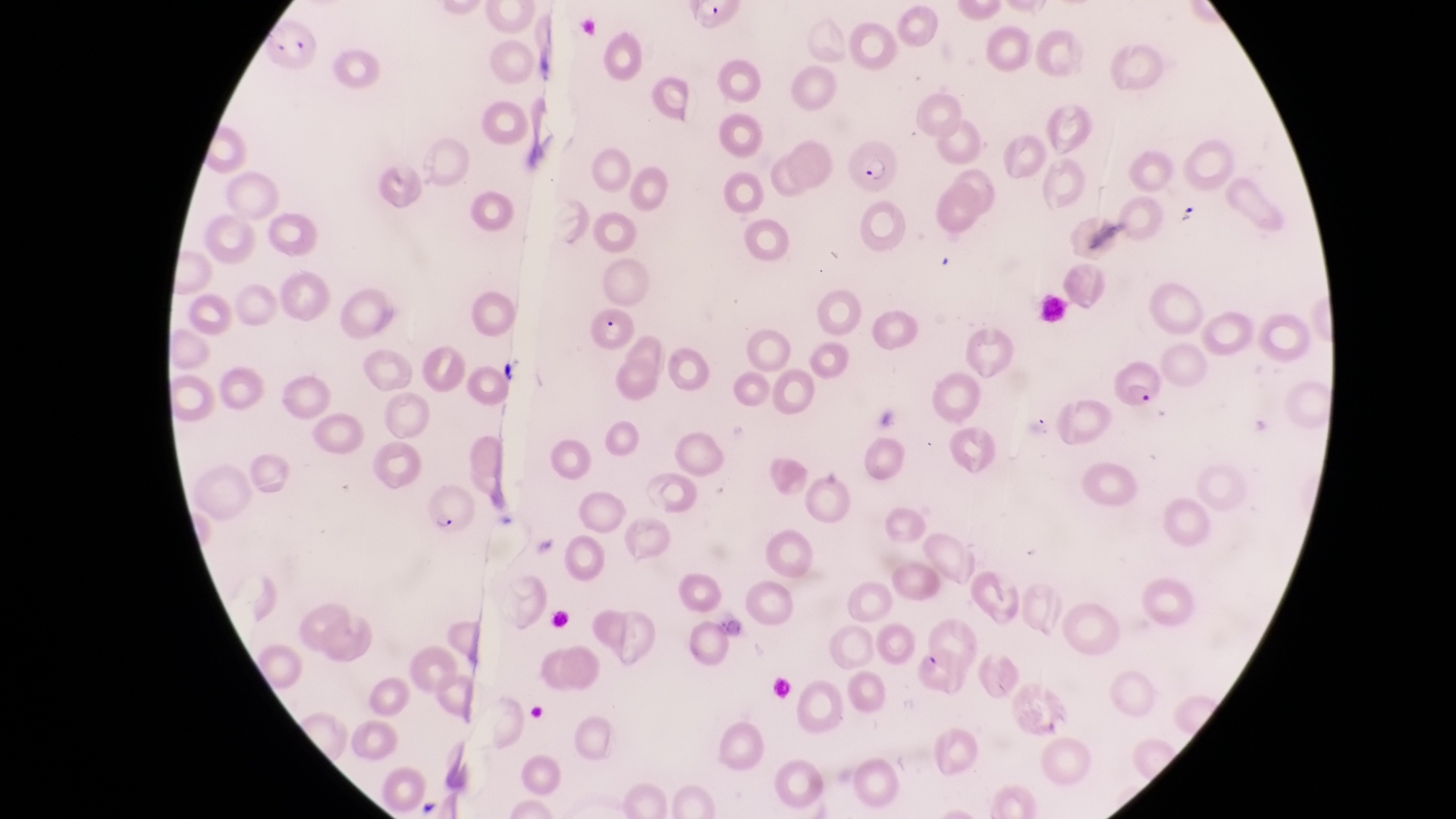

country = Uganda
parasitised red blood cell locations = approximate bounding boxes as left top right bottom in pixels: 848 145 901 194; 588 306 640 353; 1115 362 1164 415; 423 485 479 538
capture = smartphone photograph through the eyepiece of an Olympus CX-23 microscope
image size = 1456×819 pixels
magnification = 1000x
preparation = thin blood film
field of view = single